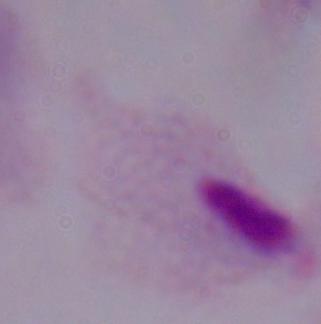

modality = micrograph
magnification = 1000x
identification = trichomonad